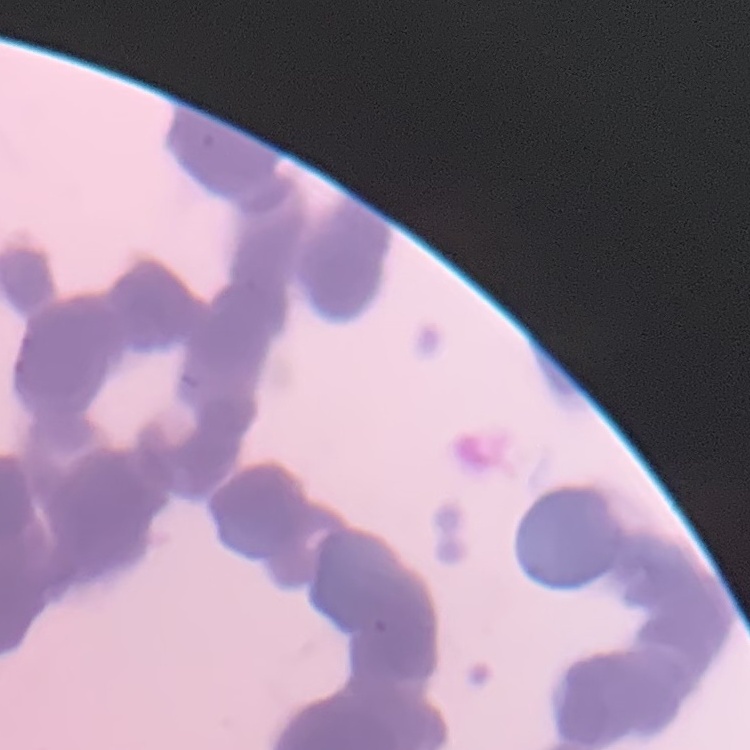

The erythrocytes exhibit rouleaux formation. Square crop of a larger photomicrograph. Thin blood film. Stained with either Field's or Giemsa.